Locate every leukocyte (white blood cell).
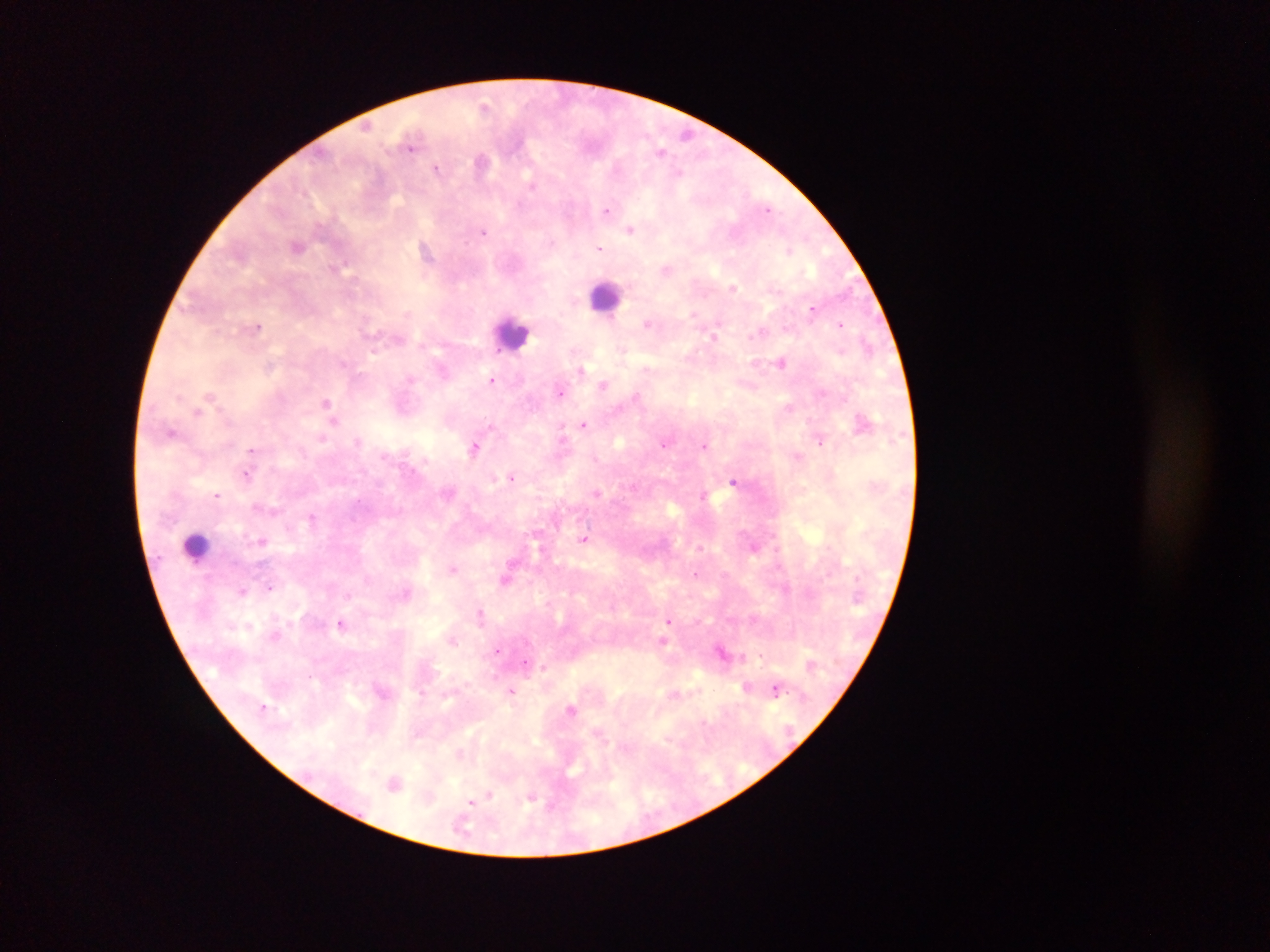
Approximate centers as x y in pixels.
Leukocytes: 607 298; 512 333; 196 546.

preparation = thick blood smear
country = Ghana
malaria parasite locations = approximate centers as x y in pixels: 484 105; 687 135; 411 146; 661 151; 481 161; 436 168; 680 172; 531 185; 768 208; 606 210; 631 229; 484 232; 297 246; 599 248; 426 251; 789 251; 666 269; 733 287; 812 310; 693 314; 647 323; 841 324; 258 328; 761 332; 714 335; 867 345; 782 362; 581 369; 492 380; 603 385; 560 393; 636 396; 326 402; 788 407; 198 412; 334 421; 583 424; 172 432; 562 434; 322 438; 358 441; 819 443; 664 445; 704 445; 474 448; 251 450; 247 475; 512 477; 733 482; 633 487; 597 493; 703 494; 217 495; 312 517; 584 539; 262 542; 699 547; 453 569; 695 574; 505 579; 270 587; 242 590; 481 614; 668 620; 341 623; 452 640; 663 640; 498 651; 722 652; 761 656; 526 664; 545 668; 747 687; 776 689; 511 691; 572 709; 460 753; 395 782; 488 797; 531 798; 472 801
field of view = single
capture = mobile-phone photograph through a microscope
image size = 1270×952 pixels